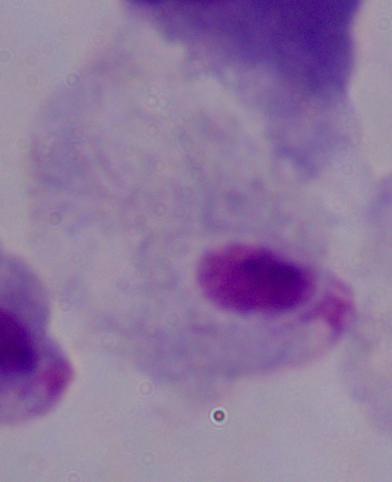
identification = trichomonad
magnification = 1000x
modality = micrograph